Assess this cell for malaria.
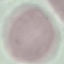

Uninfected.

{
  "preparation": "thin smear",
  "capture": "smartphone camera at the microscope eyepiece",
  "image_type": "cell patch, automatically extracted from a larger field of view and resized to 64 × 64 pixels",
  "stain": "Giemsa"
}